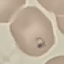
Malaria status: parasitized. Thin blood smear. Cell patch, automatically extracted from a larger field of view and resized to 64 × 64 pixels. Photographed with a smartphone camera at the microscope eyepiece. Giemsa-stained preparation.